Point out every Plasmodium parasite and every leukocyte.
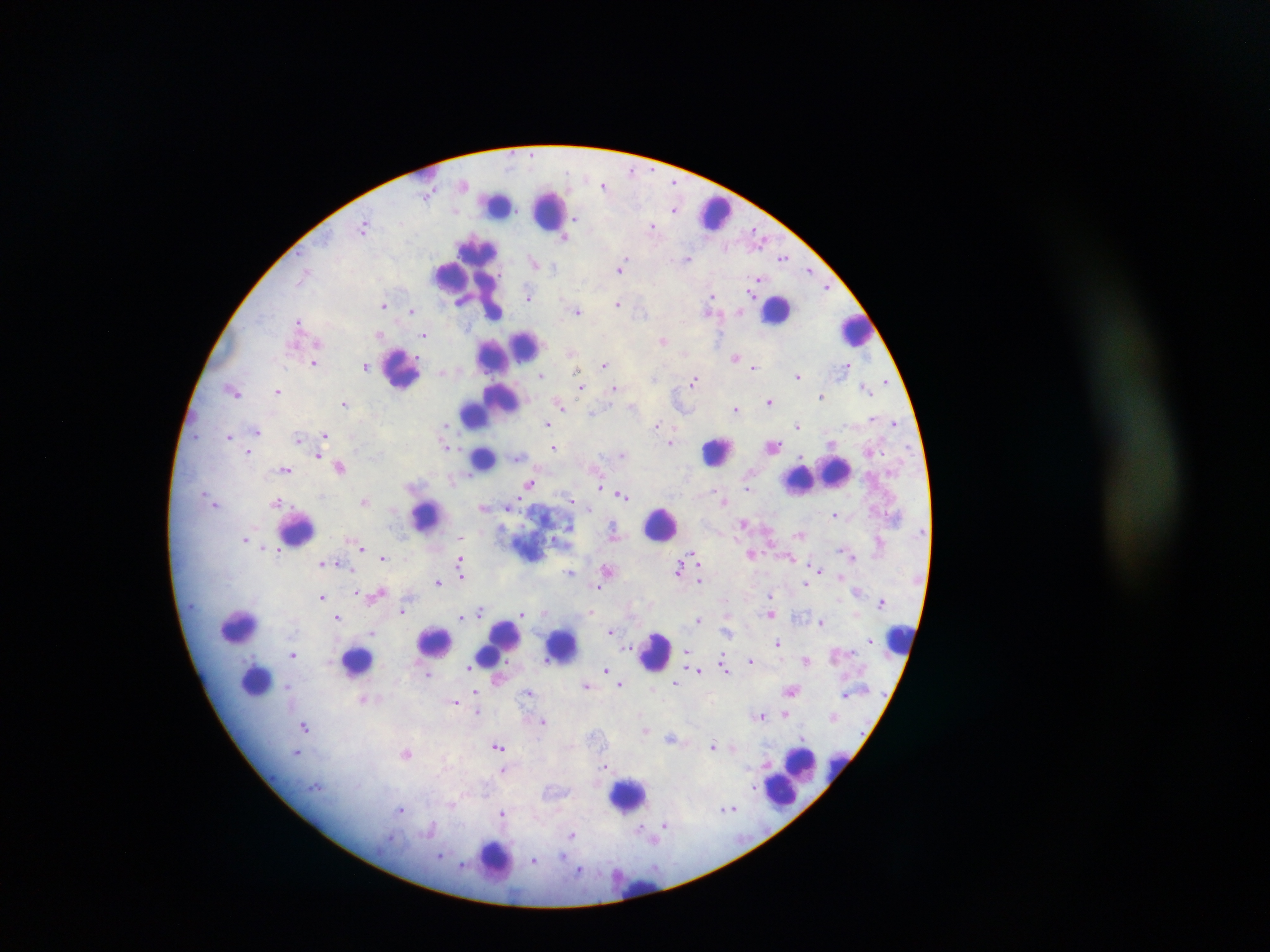

Approximate centers as [x, y] in pixels.
Plasmodium parasites: [632, 170], [605, 186], [675, 208], [576, 218], [365, 227], [653, 227], [566, 237], [687, 257], [783, 257], [535, 263], [621, 267], [810, 268], [759, 280], [828, 287], [528, 295], [713, 297], [617, 303], [385, 305], [577, 311], [741, 311], [412, 312], [711, 312], [299, 322], [380, 334], [425, 334], [664, 340], [571, 351], [735, 357], [315, 363], [606, 364], [366, 366], [754, 366], [848, 366], [442, 372], [798, 374], [542, 376], [885, 380], [694, 381], [582, 386], [865, 387], [616, 388], [234, 391], [278, 392], [821, 396], [769, 400], [561, 402], [345, 404], [632, 407], [736, 407], [591, 414], [895, 423], [446, 424], [548, 424], [657, 424], [797, 424], [257, 431], [325, 435], [230, 436], [298, 439], [671, 442], [831, 443], [446, 445], [773, 445], [554, 447], [249, 452], [623, 454], [319, 456], [517, 456], [340, 466], [286, 469], [529, 483], [600, 487], [748, 487], [622, 494], [572, 500], [364, 501], [216, 502], [576, 502], [726, 502], [277, 503], [484, 506], [510, 506], [835, 514], [743, 523], [615, 533], [800, 534], [461, 536], [246, 538], [879, 540], [267, 546], [362, 548], [279, 550], [752, 553], [694, 555], [852, 555], [384, 557], [791, 559], [460, 561], [698, 561], [337, 562], [321, 563], [680, 567], [608, 569], [819, 569], [570, 572], [462, 574], [841, 574], [699, 578], [438, 582], [805, 583], [598, 586], [356, 592], [380, 593], [770, 595], [323, 596], [882, 600], [403, 610], [591, 611], [481, 612], [543, 612], [522, 614], [772, 614], [337, 616], [461, 616], [698, 621], [821, 622], [610, 630], [372, 631], [726, 631], [869, 640], [778, 642], [627, 646], [686, 651], [293, 654], [751, 661], [806, 661], [724, 665], [471, 668], [607, 669], [699, 670], [725, 671], [429, 673], [497, 679], [677, 682], [587, 685], [621, 685], [290, 686], [791, 690], [475, 692], [529, 693], [846, 694], [363, 699], [456, 702], [478, 712], [785, 713], [761, 716], [833, 716], [544, 721], [306, 726], [646, 730], [672, 738], [498, 745], [713, 746], [733, 748], [297, 752], [408, 752], [606, 765], [503, 769], [753, 788], [728, 807], [402, 809], [503, 813], [665, 826], [574, 835], [441, 854], [535, 861], [464, 864], [579, 870].
Leukocytes: [428, 174], [497, 204], [549, 210], [714, 212], [452, 275], [468, 275], [777, 309], [494, 312], [854, 329], [516, 349], [494, 355], [402, 368], [490, 404], [475, 412], [717, 452], [475, 459], [834, 471], [816, 476], [800, 479], [426, 516], [661, 524], [296, 528], [240, 625], [900, 639], [435, 642], [497, 643], [561, 645], [490, 651], [655, 652], [357, 661], [257, 679], [803, 764], [837, 768], [791, 775], [628, 795], [496, 860], [644, 889].

Summary:
  - Image size: 1270×952 pixels
  - Country: Ghana
  - Field of view: single
  - Capture: mobile-phone photograph through a microscope
  - Preparation: thick blood film